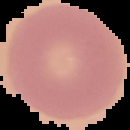
Summary:
  - Image type: segmented cell region with the area outside set to black
  - Image size: 130×130 pixels
  - Preparation: thin blood smear
  - Result: no malaria parasites seen